Name the parasite shown.
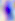

Toxoplasma gondii.

Summary:
  - Magnification: 400x
  - Modality: micrograph